Identify the cell.
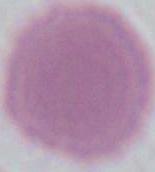
An erythrocyte.

magnification: 1000x
modality: micrograph